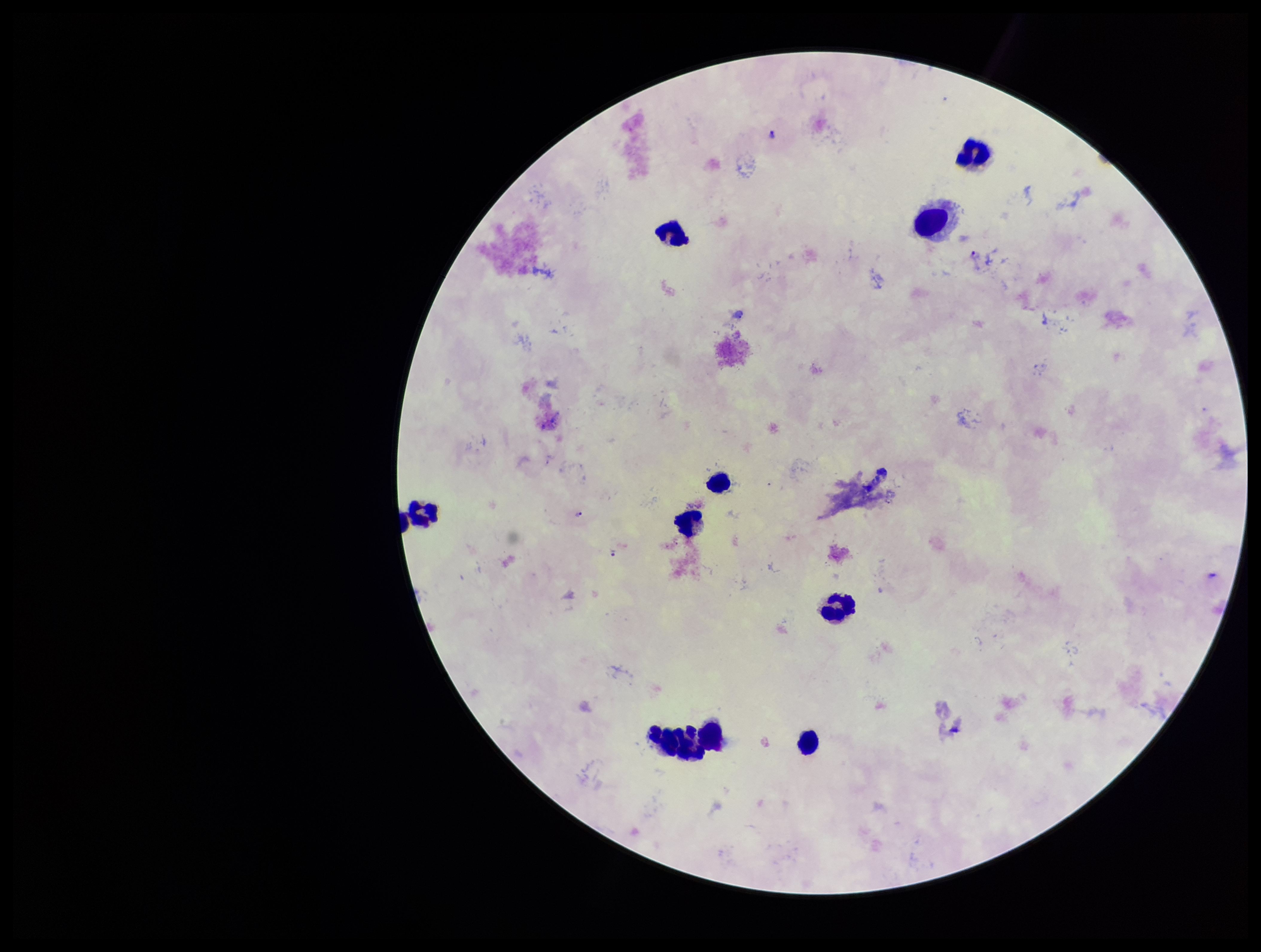
image_size: 1261×952 pixels
plasmodium_parasites: identified
patient_malaria_status: positive
stain: Giemsa
capture: smartphone photograph through the microscope eyepiece
species_reported_for_this_patient: Plasmodium falciparum
leukocyte_count: 10
preparation: thick blood smear
field_of_view: single
parasite_count: 5